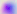
Summary:
  - Modality: photomicrograph
  - Magnification: 400x
  - Identification: Toxoplasma gondii